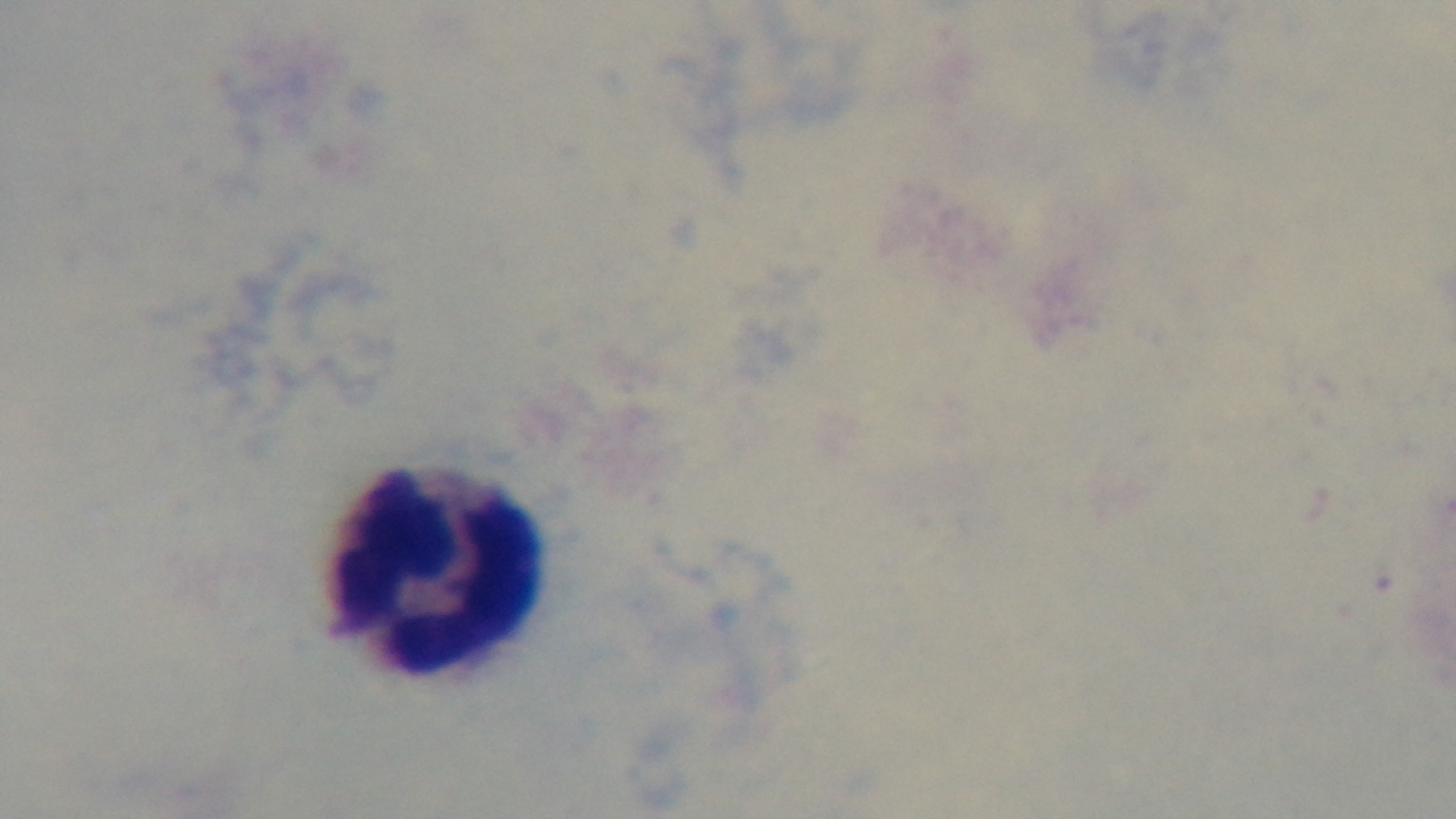
Summary:
  - Objective: 100x oil immersion
  - Malaria status: uninfected
  - Stain: Giemsa
  - Capture: mounted 4K digital camera
  - Modality: light microscopy
  - Preparation: thick blood film
  - Field of view: one from the slide